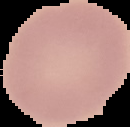

malaria status = uninfected
preparation = thin blood smear
image type = segmented cell region with the area outside set to black
image size = 130×127 pixels